Report the malaria status of this cell.
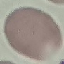

Uninfected.

Summary:
  - Stain: Giemsa
  - Capture: smartphone through the microscope eyepiece
  - Image type: cell patch, automatically extracted from a larger field of view and resized to 64 × 64 pixels
  - Preparation: thin smear